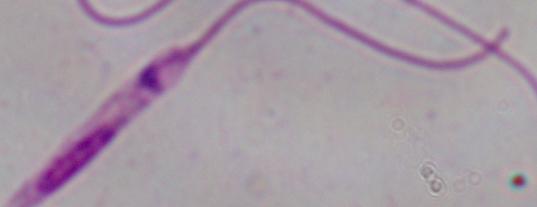
modality = micrograph
magnification = 1000x
identification = Leishmania